Report the malaria status of this cell.
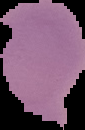
It is uninfected.

{
  "image_type": "segmented cell region with the area outside set to black",
  "image_size": "85×130 pixels",
  "preparation": "thin blood film"
}